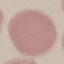
malaria_status: uninfected
stain: Giemsa
image_type: cell patch, automatically extracted from a larger field of view and resized to 64 × 64 pixels
capture: smartphone through the microscope eyepiece
preparation: thin blood smear